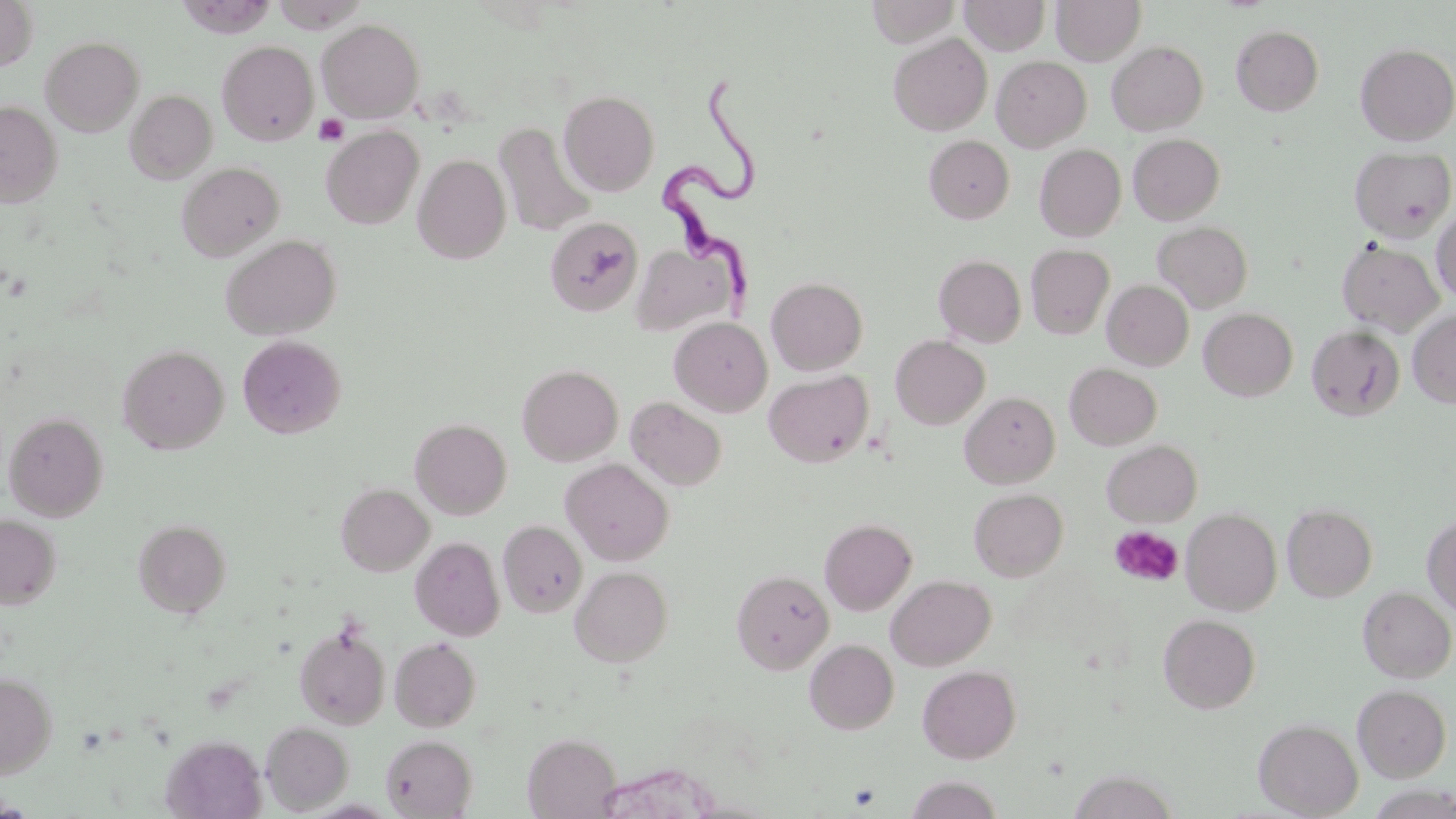

Approximate bounding boxes as named x1/y1/x2/y2 corners in pixels. Trypanosoma brucei locations: (x1=661, y1=74, x2=764, y2=309). Uninfected red blood cell locations: (x1=175, y1=0, x2=276, y2=38), (x1=272, y1=0, x2=369, y2=33), (x1=866, y1=0, x2=961, y2=47), (x1=959, y1=0, x2=1050, y2=55), (x1=1051, y1=0, x2=1145, y2=64), (x1=0, y1=1, x2=39, y2=70), (x1=317, y1=19, x2=425, y2=122), (x1=1231, y1=25, x2=1324, y2=115), (x1=888, y1=33, x2=992, y2=135), (x1=41, y1=36, x2=144, y2=136), (x1=218, y1=40, x2=318, y2=145), (x1=1107, y1=41, x2=1208, y2=135), (x1=1355, y1=43, x2=1456, y2=144), (x1=992, y1=55, x2=1091, y2=152), (x1=125, y1=89, x2=217, y2=183), (x1=559, y1=90, x2=659, y2=196), (x1=0, y1=101, x2=62, y2=207), (x1=494, y1=122, x2=596, y2=237), (x1=321, y1=125, x2=424, y2=230), (x1=1128, y1=133, x2=1225, y2=224), (x1=924, y1=135, x2=1014, y2=223), (x1=1035, y1=144, x2=1126, y2=241), (x1=1350, y1=146, x2=1455, y2=241), (x1=413, y1=154, x2=511, y2=264), (x1=176, y1=162, x2=284, y2=261), (x1=1431, y1=206, x2=1456, y2=305), (x1=545, y1=217, x2=642, y2=316), (x1=1153, y1=221, x2=1253, y2=313), (x1=221, y1=234, x2=341, y2=340), (x1=1337, y1=240, x2=1444, y2=336), (x1=631, y1=243, x2=739, y2=337), (x1=1026, y1=244, x2=1115, y2=339), (x1=934, y1=254, x2=1027, y2=347), (x1=766, y1=277, x2=868, y2=375), (x1=1102, y1=280, x2=1193, y2=371), (x1=1200, y1=308, x2=1297, y2=401), (x1=1408, y1=309, x2=1456, y2=408), (x1=669, y1=317, x2=772, y2=417), (x1=1307, y1=325, x2=1405, y2=421), (x1=237, y1=334, x2=346, y2=438), (x1=890, y1=335, x2=990, y2=429), (x1=118, y1=345, x2=229, y2=454), (x1=517, y1=363, x2=623, y2=466), (x1=1064, y1=363, x2=1162, y2=449), (x1=764, y1=370, x2=873, y2=467), (x1=960, y1=391, x2=1060, y2=488), (x1=626, y1=397, x2=727, y2=491), (x1=3, y1=411, x2=109, y2=522), (x1=410, y1=418, x2=512, y2=519), (x1=1102, y1=440, x2=1202, y2=526), (x1=560, y1=458, x2=675, y2=565), (x1=336, y1=483, x2=434, y2=576), (x1=969, y1=488, x2=1068, y2=581), (x1=1282, y1=504, x2=1377, y2=602), (x1=1182, y1=508, x2=1281, y2=615), (x1=1422, y1=512, x2=1456, y2=617), (x1=0, y1=514, x2=61, y2=609), (x1=819, y1=518, x2=917, y2=615), (x1=133, y1=519, x2=231, y2=617), (x1=497, y1=520, x2=587, y2=618), (x1=410, y1=536, x2=505, y2=640), (x1=570, y1=565, x2=673, y2=666), (x1=731, y1=569, x2=834, y2=674), (x1=886, y1=574, x2=996, y2=670), (x1=1359, y1=586, x2=1455, y2=682), (x1=1158, y1=614, x2=1260, y2=713), (x1=294, y1=620, x2=391, y2=730), (x1=389, y1=636, x2=482, y2=732), (x1=805, y1=639, x2=898, y2=734), (x1=917, y1=665, x2=1021, y2=763), (x1=0, y1=673, x2=57, y2=777), (x1=1352, y1=684, x2=1451, y2=781), (x1=1254, y1=718, x2=1363, y2=817), (x1=261, y1=721, x2=354, y2=813), (x1=522, y1=733, x2=622, y2=818), (x1=380, y1=734, x2=477, y2=818), (x1=162, y1=735, x2=266, y2=818), (x1=1070, y1=769, x2=1177, y2=818), (x1=904, y1=775, x2=1004, y2=818). Platelet locations: (x1=314, y1=114, x2=349, y2=145), (x1=1109, y1=525, x2=1184, y2=587), (x1=848, y1=783, x2=881, y2=809). Slide-level diagnosis: Trypanosoma brucei. Image is 1456×819 pixels. Thin blood film. Captured at 1000x magnification. Optical microscopy. May-Grünwald-Giemsa-stained preparation. One field of a larger specimen.